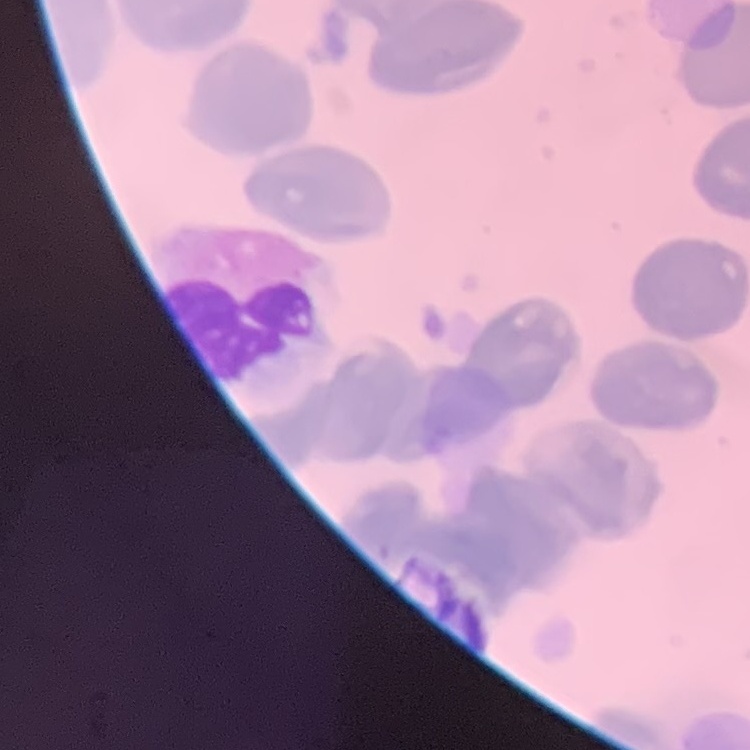 The erythrocytes exhibit no rouleaux formation. One tile cut from a larger photomicrograph. Thin peripheral smear. Stained with either Field's or Giemsa.